Look for Plasmodium parasites.
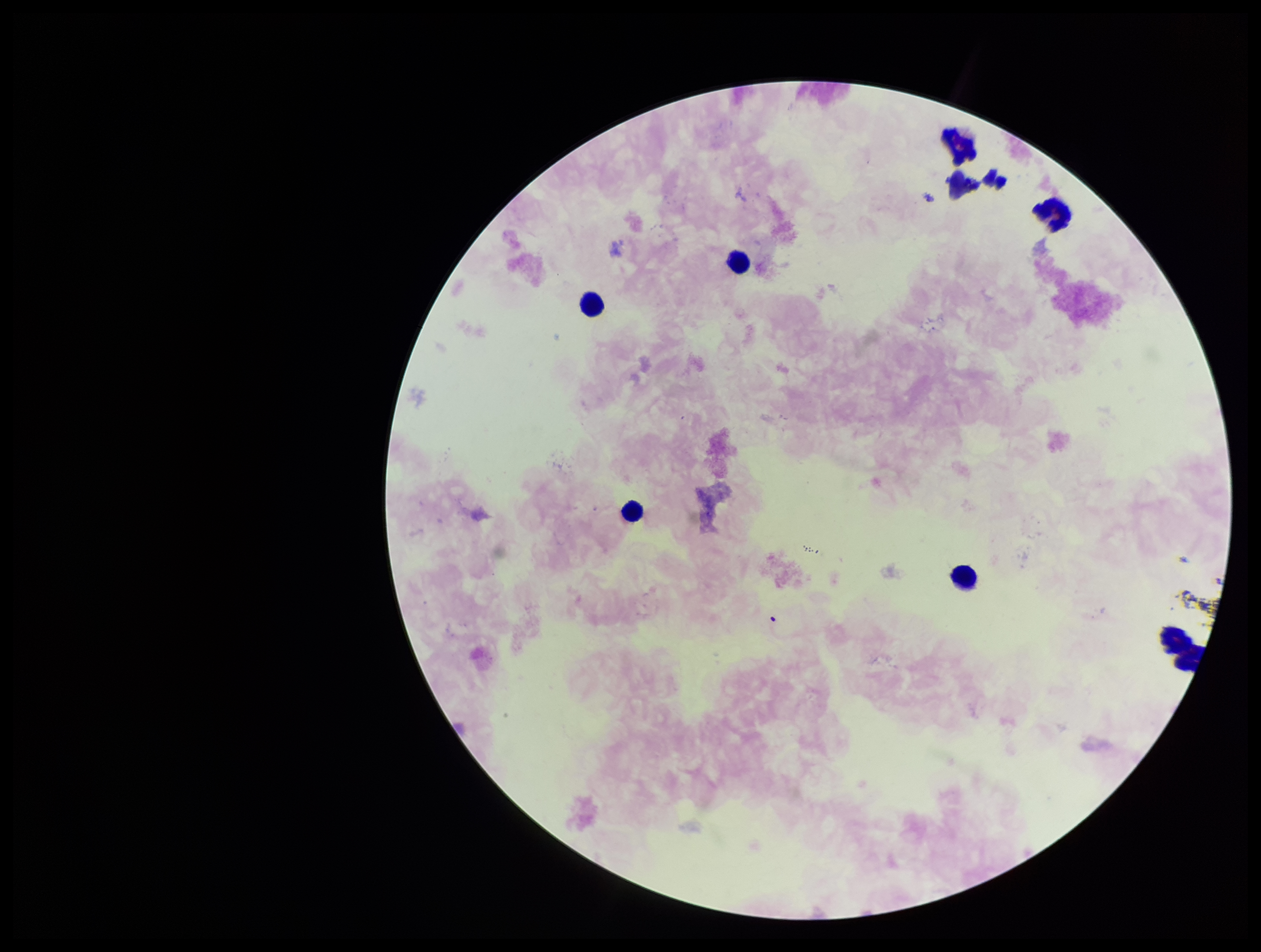

None detected.

Parasite count: 0. Patient malaria status: negative. Leukocyte count: 8. Giemsa stain. Photographed through the microscope eyepiece with a smartphone camera. Single field of view. Preparation: thick. Image is 1261×952 pixels.